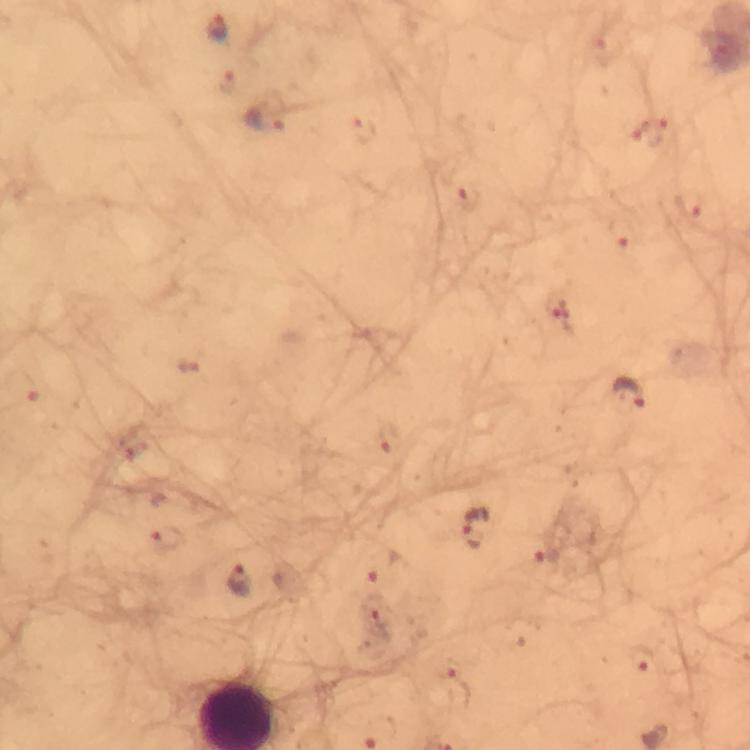

image_size: 750×750 pixels
context: from a diagnostic examination for malaria
stain: Giemsa
cropped_from: one field of view
plasmodium_parasite_locations: 'approximate centers as [x, y] in pixels: [218, 28], [607, 52], [228, 81], [266, 118], [650, 131], [363, 134], [468, 199], [690, 203], [621, 232], [557, 310], [187, 364], [628, 393], [387, 440], [475, 528], [167, 541], [547, 551], [380, 564], [240, 580], [376, 613], [641, 657], [449, 669]'
preparation: thick smear
immersion_oil: used
capture: smartphone photograph through a microscope
magnification: 100x